Describe the morphology of the red blood cells.
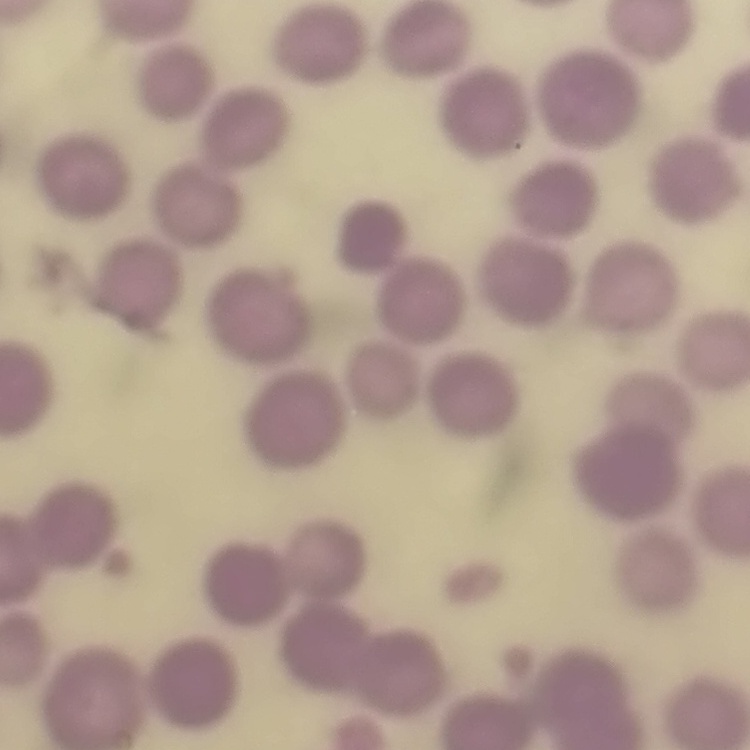

They show no rouleaux formation.

Summary:
  - Stain: Field's or Giemsa
  - Preparation: thin blood film
  - Image type: square crop of a larger photomicrograph